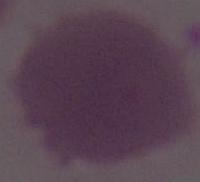
Summary:
  - Modality: micrograph
  - Magnification: 1000x
  - Identification: erythrocyte